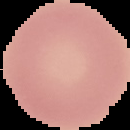 Image is 130×130 pixels. From a thin blood film. Malaria status: uninfected. Segmented cell region on a black background.